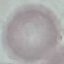

malaria_status: uninfected
capture: smartphone through the microscope eyepiece
image_type: automatically extracted cell patch, resized to 64 × 64 pixels
preparation: thin blood film
stain: Giemsa